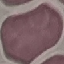

Result: no malaria parasites seen. Acquired by smartphone through the microscope eyepiece. Thin blood film. Giemsa-stained preparation. Cell patch, automatically extracted from a larger field of view and resized to 64 × 64 pixels.